Identify the preparation type.
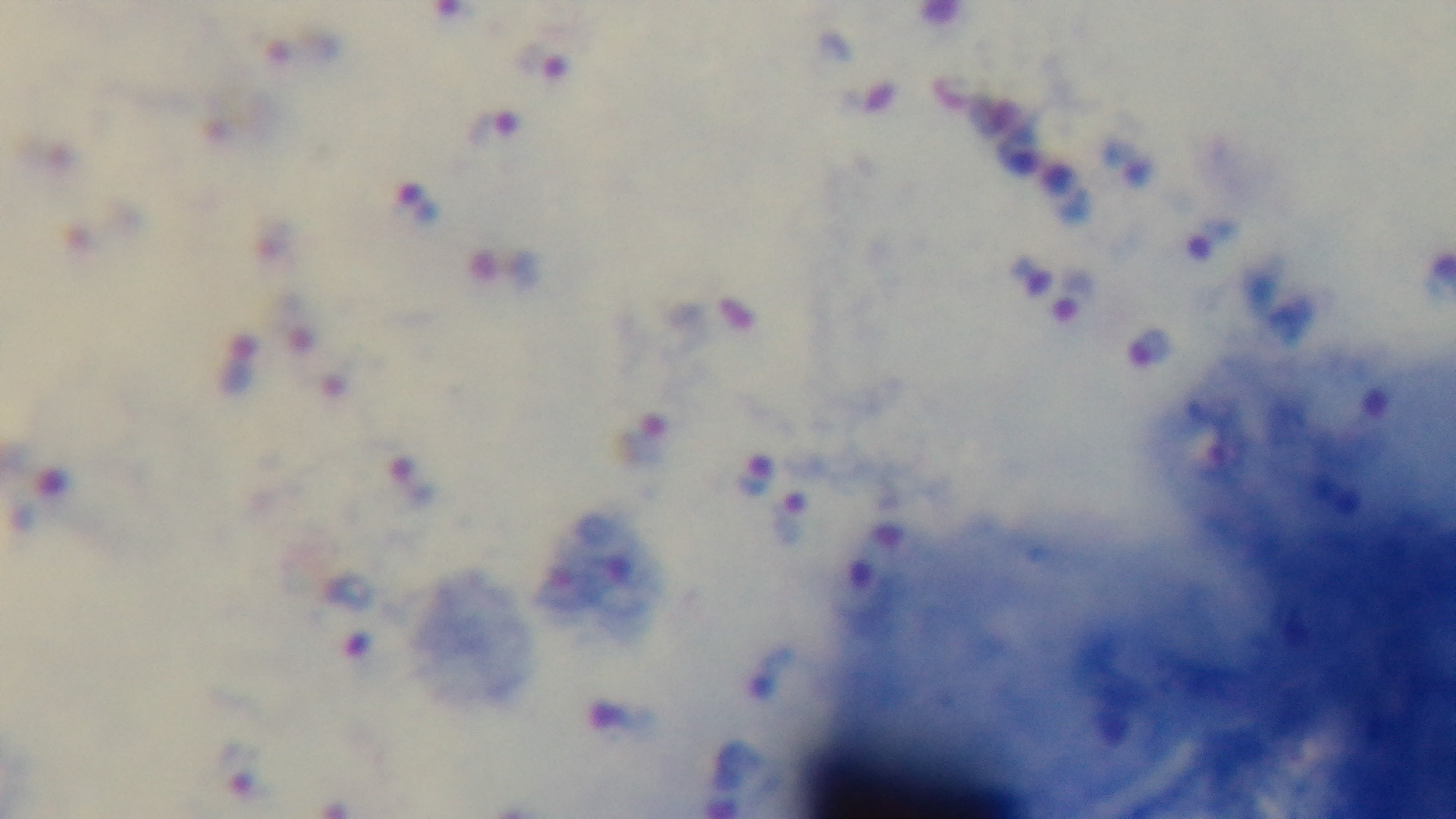

Thick.

{
  "modality": "light microscopy",
  "capture": "mounted 4K digital camera",
  "stain": "Giemsa",
  "objective": "100x oil immersion",
  "field_of_view": "single",
  "malaria_status": "infected"
}